Evaluate for malaria.
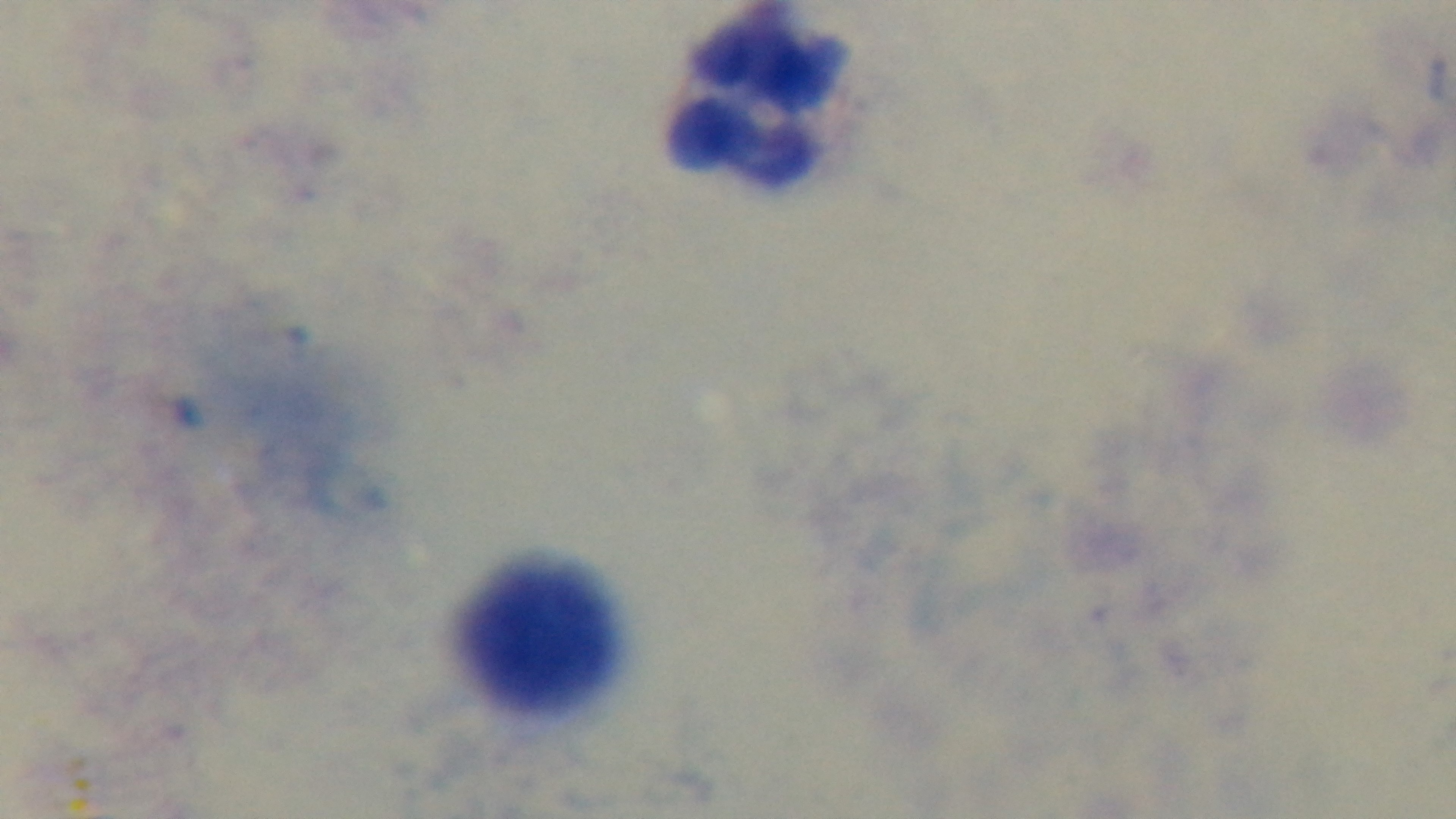

Uninfected.

Photomicrograph. Oil-immersion objective, 100x. Giemsa stain. Single field of view. Preparation: thick. Mounted 4K digital camera.